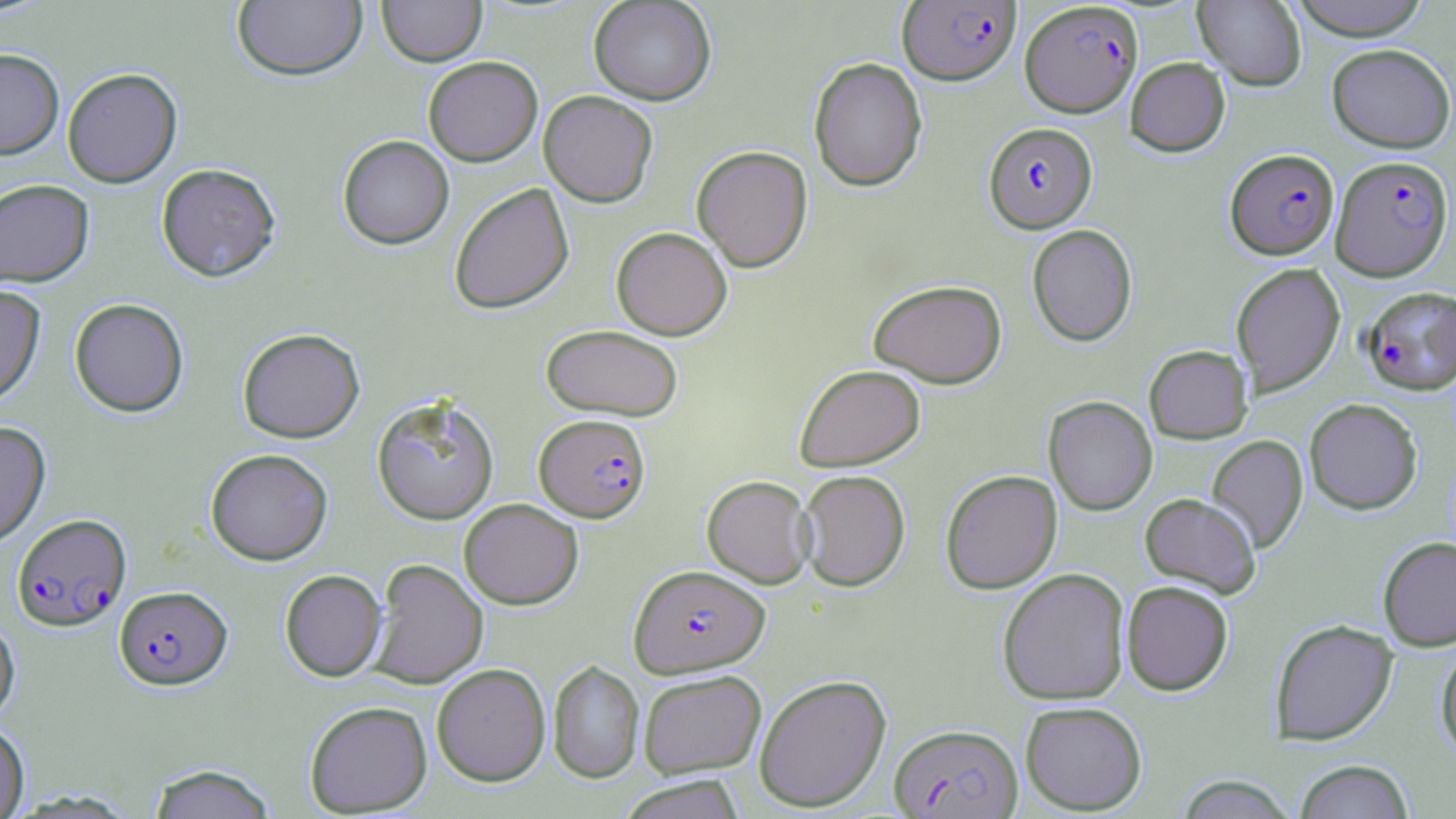
Summary:
  - Coordinate format: approximate bounding boxes as named x1/y1/x2/y2 corners in pixels
  - Plasmodium falciparum-infected red blood cell locations: (x1=898, y1=1, x2=1020, y2=85), (x1=1019, y1=1, x2=1143, y2=117), (x1=984, y1=122, x2=1096, y2=233), (x1=1226, y1=149, x2=1338, y2=259), (x1=1331, y1=154, x2=1454, y2=281), (x1=1361, y1=287, x2=1456, y2=394), (x1=535, y1=413, x2=650, y2=522), (x1=12, y1=514, x2=131, y2=630), (x1=629, y1=564, x2=770, y2=678), (x1=114, y1=585, x2=232, y2=689), (x1=889, y1=723, x2=1023, y2=818)
  - Uninfected red blood cell locations: (x1=377, y1=0, x2=487, y2=66), (x1=588, y1=0, x2=716, y2=105), (x1=1193, y1=0, x2=1306, y2=90), (x1=1288, y1=0, x2=1431, y2=40), (x1=232, y1=1, x2=367, y2=80), (x1=1326, y1=43, x2=1455, y2=152), (x1=0, y1=48, x2=64, y2=159), (x1=423, y1=56, x2=543, y2=166), (x1=808, y1=57, x2=928, y2=192), (x1=1125, y1=57, x2=1230, y2=156), (x1=62, y1=67, x2=182, y2=187), (x1=539, y1=90, x2=657, y2=207), (x1=337, y1=135, x2=454, y2=250), (x1=691, y1=145, x2=813, y2=272), (x1=156, y1=163, x2=280, y2=281), (x1=0, y1=178, x2=95, y2=287), (x1=449, y1=183, x2=574, y2=314), (x1=1027, y1=224, x2=1137, y2=346), (x1=611, y1=227, x2=732, y2=340), (x1=1230, y1=263, x2=1345, y2=396), (x1=869, y1=279, x2=1007, y2=387), (x1=0, y1=284, x2=46, y2=407), (x1=69, y1=298, x2=189, y2=417), (x1=541, y1=324, x2=684, y2=421), (x1=237, y1=328, x2=365, y2=443), (x1=1144, y1=345, x2=1253, y2=443), (x1=795, y1=363, x2=925, y2=471), (x1=371, y1=393, x2=500, y2=525), (x1=1044, y1=396, x2=1157, y2=515), (x1=1304, y1=398, x2=1423, y2=514), (x1=0, y1=421, x2=51, y2=547), (x1=1207, y1=435, x2=1309, y2=553), (x1=205, y1=448, x2=333, y2=565), (x1=796, y1=469, x2=911, y2=591), (x1=940, y1=469, x2=1062, y2=594), (x1=702, y1=475, x2=816, y2=588), (x1=1140, y1=493, x2=1261, y2=598), (x1=459, y1=498, x2=584, y2=609), (x1=1378, y1=536, x2=1456, y2=651), (x1=368, y1=558, x2=488, y2=689), (x1=997, y1=567, x2=1131, y2=705), (x1=280, y1=569, x2=386, y2=681), (x1=1121, y1=580, x2=1233, y2=695), (x1=0, y1=614, x2=20, y2=725), (x1=1270, y1=619, x2=1398, y2=745), (x1=1436, y1=642, x2=1456, y2=763), (x1=548, y1=660, x2=644, y2=783), (x1=432, y1=663, x2=550, y2=786), (x1=638, y1=669, x2=767, y2=778), (x1=753, y1=673, x2=892, y2=812), (x1=304, y1=700, x2=433, y2=816), (x1=1019, y1=701, x2=1147, y2=814), (x1=0, y1=721, x2=30, y2=818), (x1=1294, y1=759, x2=1415, y2=819), (x1=146, y1=763, x2=278, y2=819), (x1=1175, y1=774, x2=1297, y2=818), (x1=616, y1=775, x2=748, y2=818)
  - Slide-level diagnosis: Plasmodium falciparum
  - Stain: May-Grünwald-Giemsa
  - Preparation: thin blood smear
  - Modality: optical microscopy
  - Field of view: single
  - Magnification: 1000x
  - Image size: 1456×819 pixels